Name the parasite shown.
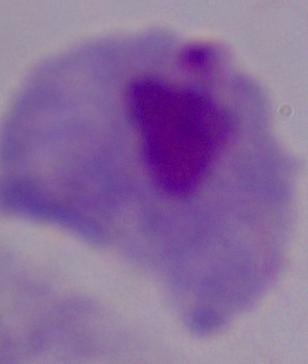
This is a trichomonad.

Summary:
  - Modality: photomicrograph
  - Magnification: 1000x